Classify this cell by malaria status.
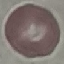

Uninfected.

Summary:
  - Stain: Giemsa
  - Capture: smartphone camera at the microscope eyepiece
  - Image type: cell patch, automatically extracted from a larger field of view and resized to 64 × 64 pixels
  - Preparation: thin smear